Locate every leukocyte (white blood cell).
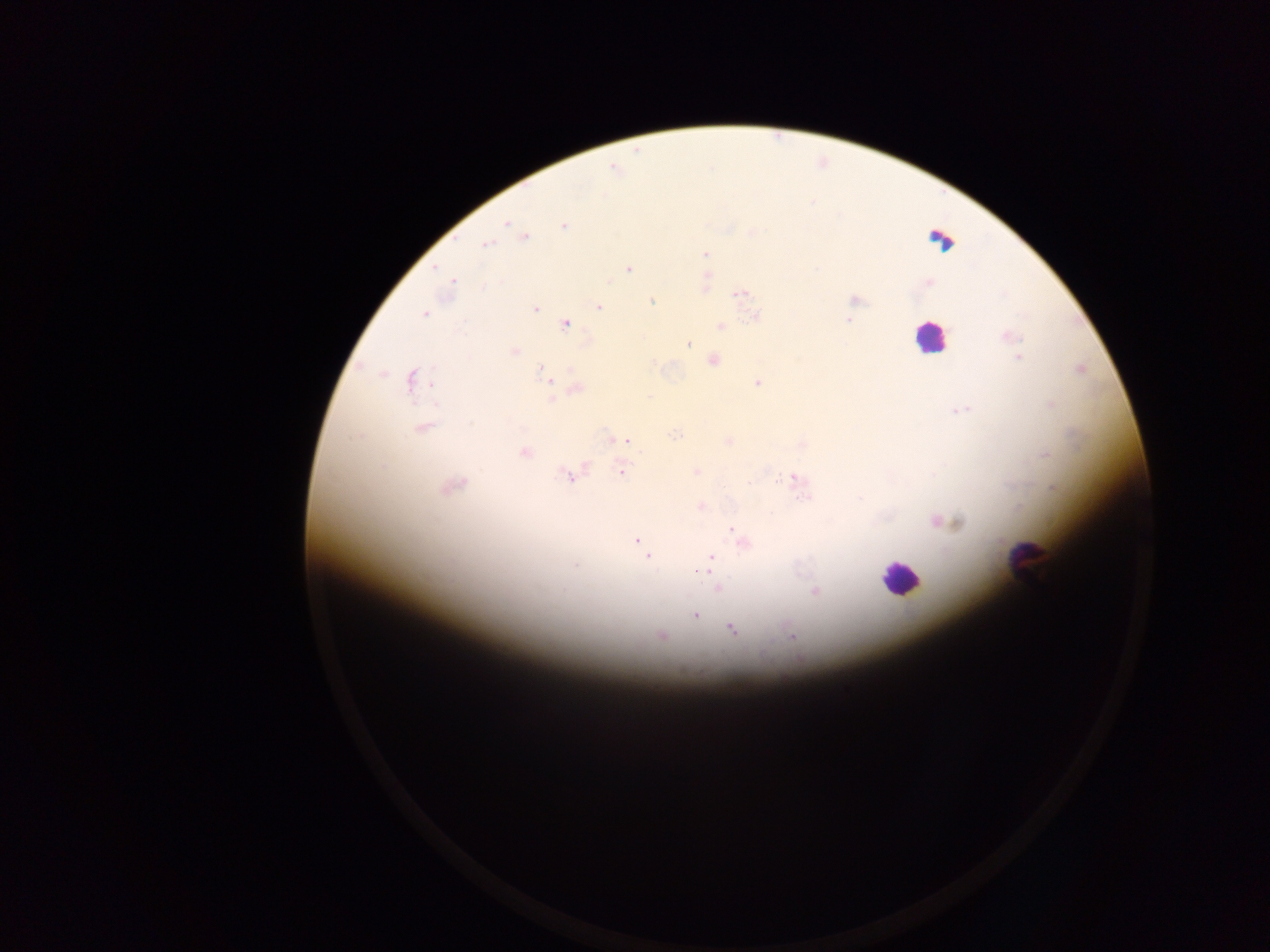

Approximate centers as (x, y) in pixels.
Leukocytes: (941, 241), (930, 338), (1027, 562), (900, 577).

image_size: 1270×952 pixels
field_of_view: single
country: Ghana
preparation: thick blood film
malaria_parasite_locations: 'approximate centers as (x, y) in pixels: (614, 168), (505, 221), (564, 225), (524, 236), (487, 244), (705, 254), (628, 268), (706, 281), (928, 281), (452, 283), (739, 294), (853, 300), (652, 301), (598, 306), (534, 309), (424, 313), (852, 314), (755, 316), (850, 320), (565, 323), (719, 326), (1009, 337), (688, 343), (514, 351), (1019, 357), (712, 359), (655, 361), (1079, 369), (546, 374), (412, 380), (548, 382), (758, 382), (575, 388), (1050, 404), (959, 408), (422, 428), (676, 435), (617, 439), (727, 441), (802, 443), (523, 452), (622, 469), (696, 471), (570, 475), (794, 480), (451, 484), (1052, 488), (701, 506), (940, 521), (733, 527), (638, 541), (741, 541), (642, 544), (648, 557), (711, 559), (717, 589), (814, 591), (694, 614), (731, 628), (661, 635), (790, 635)'
capture: mobile-phone photograph through a microscope